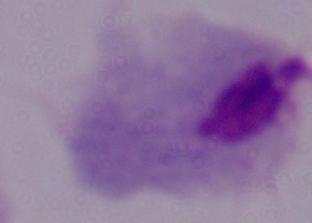
Summary:
  - Magnification: 1000x
  - Modality: photomicrograph
  - Identification: trichomonad